Locate every blood parasite and identify its species.
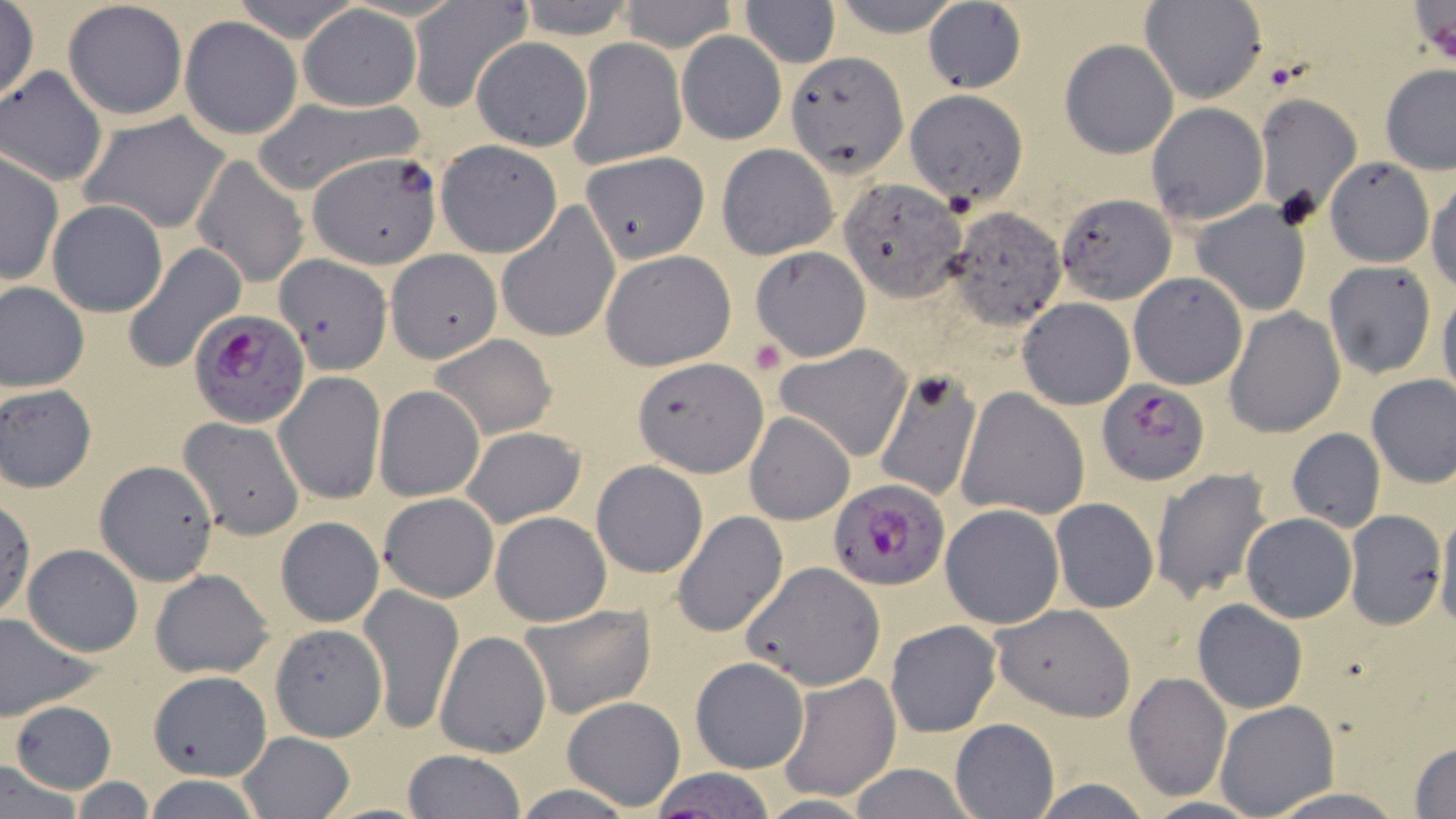

Approximate bounding boxes as named x1/y1/x2/y2 corners in pixels.
Plasmodium falciparum-infected red blood cells: (x1=186, y1=307, x2=311, y2=428), (x1=1096, y1=378, x2=1208, y2=485), (x1=828, y1=481, x2=949, y2=591).
No Plasmodium ovale, Plasmodium malariae, Plasmodium vivax, Babesia divergens, or Trypanosoma brucei observed.

Uninfected red blood cell locations: (x1=513, y1=0, x2=637, y2=38), (x1=615, y1=0, x2=738, y2=52), (x1=835, y1=0, x2=958, y2=35), (x1=409, y1=1, x2=532, y2=110), (x1=63, y1=2, x2=187, y2=120), (x1=741, y1=2, x2=839, y2=66), (x1=921, y1=2, x2=1027, y2=93), (x1=1140, y1=2, x2=1265, y2=105), (x1=0, y1=3, x2=40, y2=105), (x1=298, y1=5, x2=421, y2=111), (x1=179, y1=17, x2=303, y2=140), (x1=677, y1=31, x2=785, y2=145), (x1=471, y1=36, x2=591, y2=150), (x1=568, y1=38, x2=685, y2=169), (x1=1060, y1=38, x2=1179, y2=157), (x1=788, y1=50, x2=907, y2=173), (x1=0, y1=65, x2=108, y2=186), (x1=1380, y1=65, x2=1456, y2=174), (x1=906, y1=88, x2=1027, y2=205), (x1=1252, y1=91, x2=1363, y2=219), (x1=246, y1=96, x2=427, y2=197), (x1=1146, y1=101, x2=1267, y2=224), (x1=80, y1=112, x2=232, y2=233), (x1=435, y1=140, x2=562, y2=257), (x1=716, y1=143, x2=838, y2=260), (x1=0, y1=150, x2=63, y2=286), (x1=307, y1=151, x2=440, y2=268), (x1=581, y1=152, x2=709, y2=264), (x1=191, y1=153, x2=311, y2=288), (x1=1325, y1=160, x2=1434, y2=266), (x1=1427, y1=177, x2=1456, y2=292), (x1=839, y1=179, x2=967, y2=300), (x1=1055, y1=194, x2=1177, y2=305), (x1=46, y1=199, x2=169, y2=318), (x1=1192, y1=201, x2=1312, y2=316), (x1=495, y1=202, x2=620, y2=344), (x1=943, y1=209, x2=1065, y2=330), (x1=121, y1=243, x2=246, y2=370), (x1=751, y1=245, x2=870, y2=360), (x1=387, y1=249, x2=502, y2=361), (x1=599, y1=250, x2=736, y2=371), (x1=277, y1=253, x2=390, y2=373), (x1=1323, y1=261, x2=1435, y2=379), (x1=1128, y1=273, x2=1248, y2=390), (x1=0, y1=281, x2=88, y2=393), (x1=1437, y1=292, x2=1456, y2=410), (x1=1017, y1=298, x2=1135, y2=410), (x1=1223, y1=307, x2=1346, y2=437), (x1=429, y1=333, x2=558, y2=439), (x1=775, y1=344, x2=914, y2=462), (x1=635, y1=357, x2=768, y2=478), (x1=871, y1=368, x2=982, y2=504), (x1=275, y1=371, x2=386, y2=505), (x1=1365, y1=375, x2=1456, y2=488), (x1=1, y1=384, x2=99, y2=492), (x1=374, y1=385, x2=485, y2=501), (x1=957, y1=388, x2=1090, y2=520), (x1=744, y1=412, x2=854, y2=525), (x1=177, y1=415, x2=306, y2=538), (x1=460, y1=426, x2=586, y2=528), (x1=1286, y1=429, x2=1385, y2=532), (x1=94, y1=460, x2=220, y2=588), (x1=592, y1=460, x2=709, y2=579), (x1=1151, y1=466, x2=1273, y2=605), (x1=379, y1=492, x2=498, y2=602), (x1=0, y1=498, x2=35, y2=621), (x1=1051, y1=498, x2=1158, y2=612), (x1=940, y1=503, x2=1065, y2=629), (x1=1435, y1=506, x2=1456, y2=633), (x1=1344, y1=508, x2=1447, y2=631), (x1=489, y1=510, x2=612, y2=627), (x1=672, y1=512, x2=788, y2=636), (x1=1241, y1=513, x2=1356, y2=623), (x1=274, y1=518, x2=383, y2=630), (x1=21, y1=542, x2=144, y2=656), (x1=741, y1=562, x2=884, y2=692), (x1=149, y1=567, x2=274, y2=679), (x1=359, y1=584, x2=464, y2=735), (x1=1194, y1=599, x2=1307, y2=713), (x1=519, y1=602, x2=656, y2=719), (x1=991, y1=602, x2=1137, y2=721), (x1=0, y1=610, x2=102, y2=718), (x1=886, y1=620, x2=1003, y2=738), (x1=269, y1=624, x2=387, y2=742), (x1=435, y1=630, x2=553, y2=758), (x1=817, y1=631, x2=956, y2=766), (x1=690, y1=656, x2=809, y2=774), (x1=150, y1=670, x2=271, y2=781), (x1=1124, y1=671, x2=1231, y2=800), (x1=780, y1=673, x2=900, y2=799), (x1=562, y1=696, x2=687, y2=812), (x1=9, y1=699, x2=116, y2=793), (x1=1215, y1=700, x2=1339, y2=817), (x1=950, y1=718, x2=1059, y2=818), (x1=237, y1=731, x2=357, y2=819), (x1=1410, y1=741, x2=1456, y2=817), (x1=400, y1=750, x2=526, y2=819), (x1=0, y1=759, x2=85, y2=817), (x1=848, y1=765, x2=978, y2=819), (x1=644, y1=769, x2=782, y2=818), (x1=140, y1=775, x2=267, y2=817), (x1=62, y1=778, x2=158, y2=815), (x1=1024, y1=778, x2=1158, y2=818), (x1=1265, y1=787, x2=1407, y2=818), (x1=1134, y1=797, x2=1268, y2=818). Platelet locations: (x1=750, y1=339, x2=788, y2=376). Slide-level diagnosis: Plasmodium falciparum. 1000x magnification. Thin blood film. One field of a larger specimen. May-Grünwald-Giemsa stain. Optical microscopy. Image is 1456×819 pixels.